Assess the morphology of the erythrocytes.
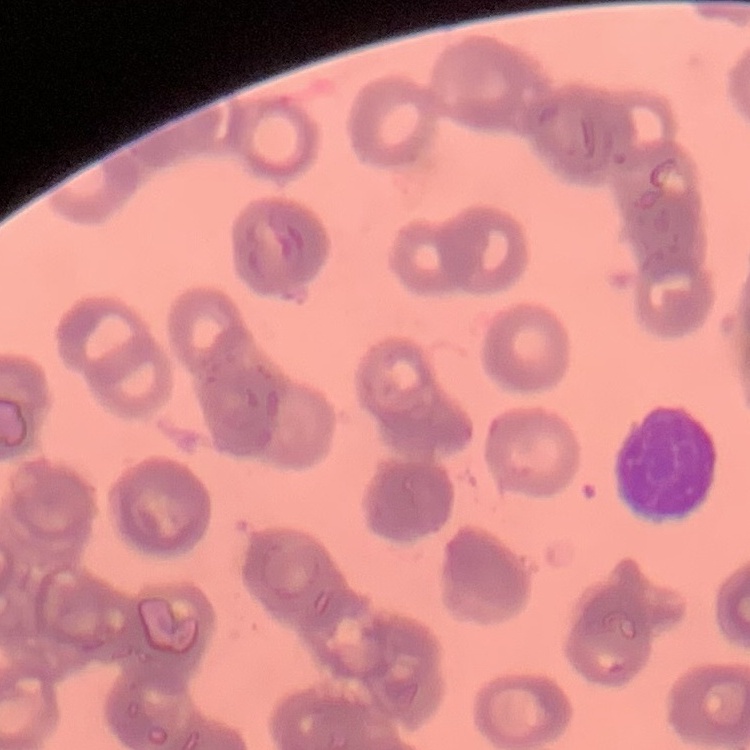

They show rouleaux formation.

image type = square crop of a larger photomicrograph
stain = Field's or Giemsa
preparation = thin blood film